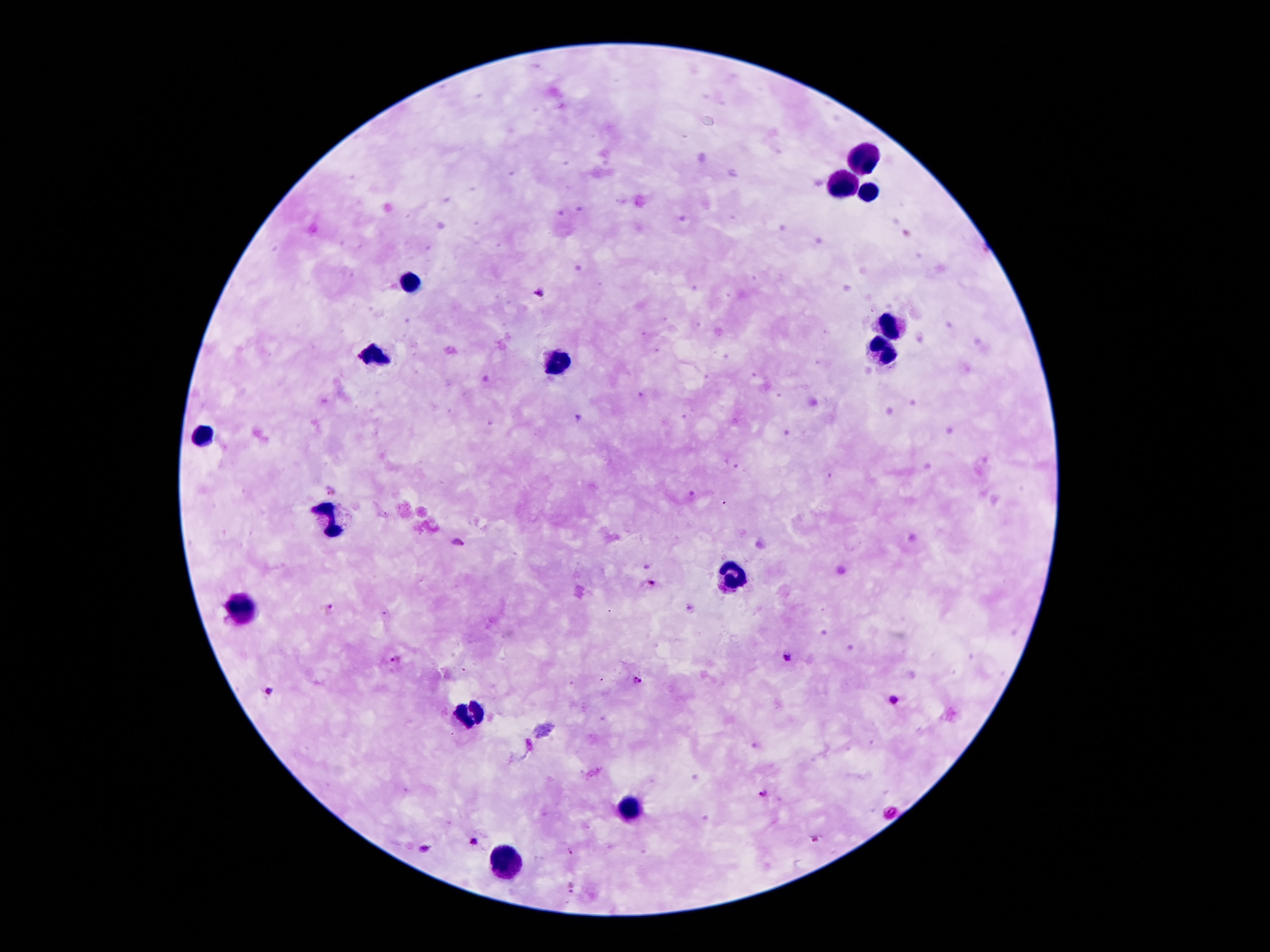

plasmodium_parasite_locations: 'approximate object centers, in pixels from the top-left corner: (x=538, y=293), (x=457, y=543), (x=648, y=567), (x=653, y=583), (x=328, y=609), (x=787, y=657), (x=396, y=659), (x=636, y=681), (x=270, y=690), (x=895, y=701), (x=762, y=793), (x=892, y=814), (x=814, y=839), (x=473, y=842), (x=424, y=850), (x=571, y=886)'
field_of_view: one from this slide
patient_malaria_status: positive for Plasmodium falciparum
stain: Giemsa
magnification: 100x
preparation: thick blood smear
capture: smartphone camera through the microscope eyepiece
image_size: 1270×952 pixels
leukocyte_locations: 'approximate object centers, in pixels from the top-left corner: (x=864, y=161), (x=845, y=183), (x=868, y=194), (x=408, y=281), (x=895, y=327), (x=883, y=352), (x=379, y=354), (x=564, y=365), (x=200, y=435), (x=335, y=519), (x=734, y=574), (x=244, y=607), (x=471, y=714), (x=631, y=811), (x=505, y=861)'